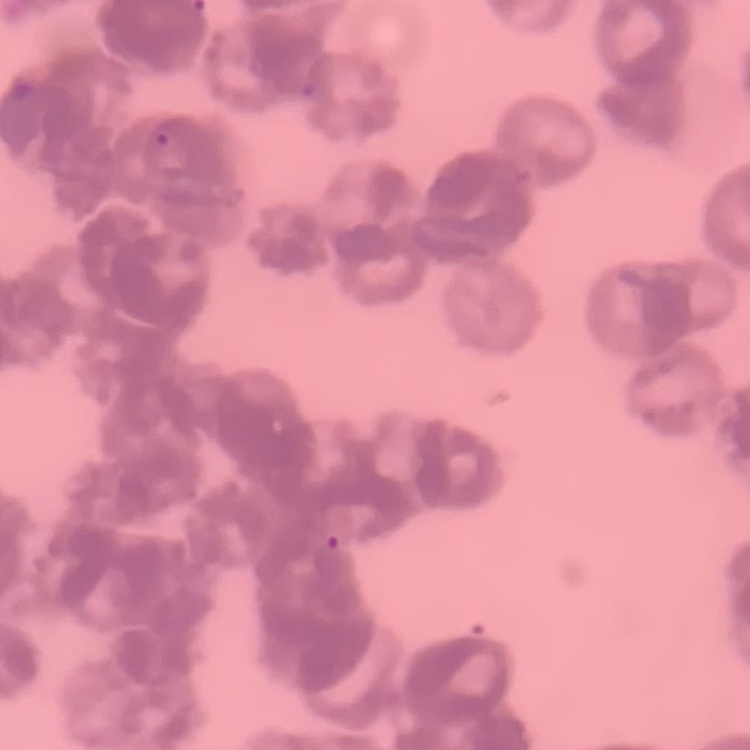
The red blood cells show rouleaux formation. Square crop of a larger photomicrograph. Thin blood smear. Field's or Giemsa stain.